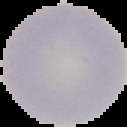

malaria status = uninfected
image type = cell region segmented out of the field of view; surrounding area masked to black
image size = 127×127 pixels
preparation = thin blood film